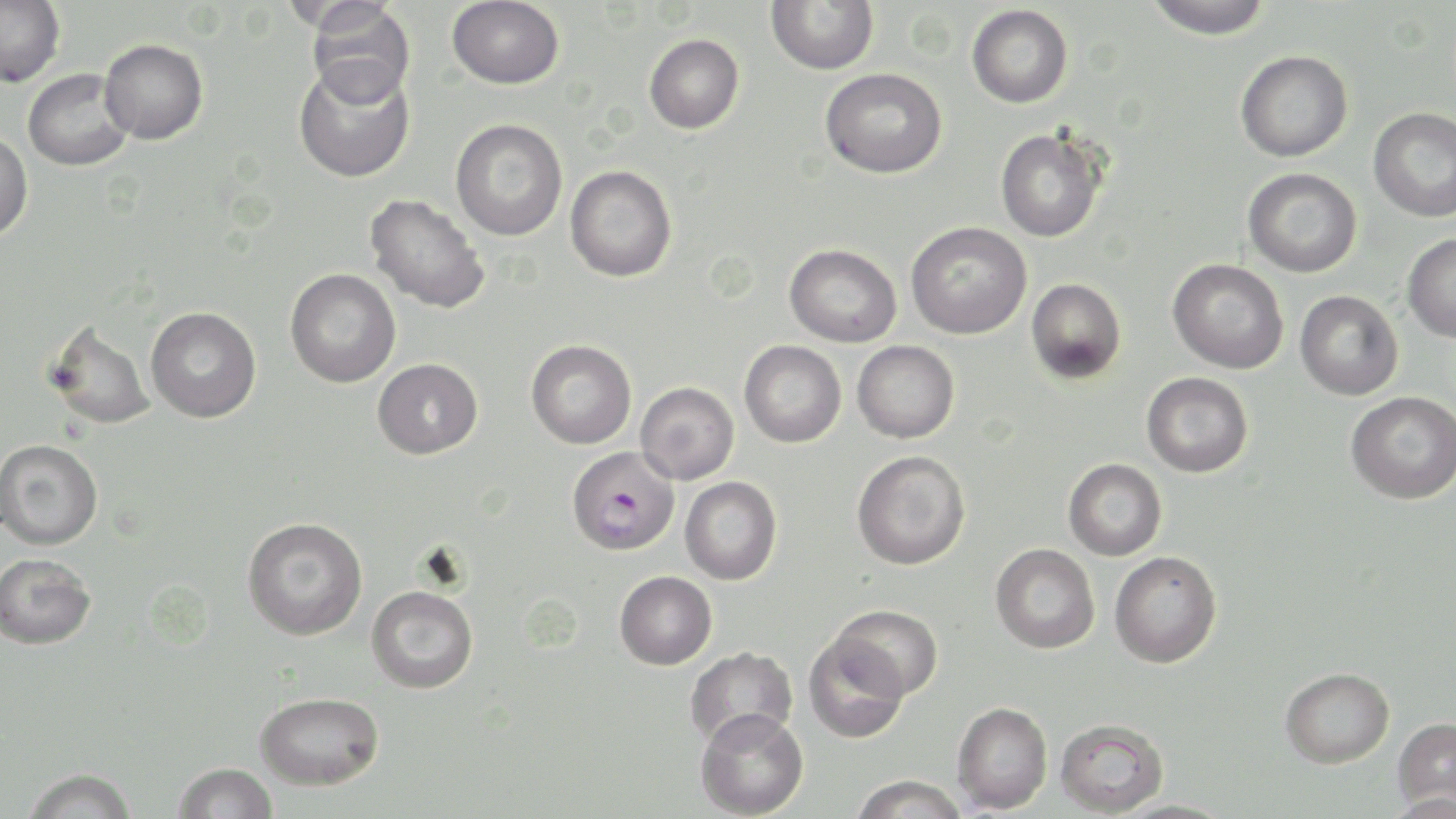
slide-level diagnosis = Plasmodium falciparum
modality = light microscopy
Plasmodium falciparum-infected red blood cell locations = approximate bounding boxes as (x1, y1, x2, y2) in pixels: (567, 446, 680, 556)
preparation = thin blood smear
magnification = 1000x
field of view = single
image size = 1456×819 pixels
stain = May-Grünwald-Giemsa
uninfected red blood cell locations = approximate bounding boxes as (x1, y1, x2, y2) in pixels: (447, 0, 564, 89), (766, 0, 879, 75), (1141, 0, 1274, 40), (0, 1, 65, 87), (305, 2, 416, 105), (966, 4, 1073, 108), (644, 33, 745, 133), (100, 39, 208, 144), (1235, 49, 1353, 162), (293, 62, 415, 183), (819, 67, 948, 178), (23, 68, 134, 171), (1369, 107, 1456, 222), (450, 118, 568, 241), (995, 127, 1108, 242), (0, 130, 33, 242), (565, 165, 677, 282), (1242, 167, 1362, 277), (364, 195, 490, 314), (906, 222, 1032, 339), (1402, 233, 1456, 343), (784, 244, 902, 348), (1167, 258, 1289, 374), (285, 269, 401, 388), (1026, 278, 1127, 384), (1295, 290, 1403, 400), (145, 307, 261, 423), (43, 319, 156, 430), (526, 340, 637, 449), (739, 340, 847, 448), (852, 340, 960, 443), (372, 359, 483, 459), (1141, 372, 1253, 477), (635, 382, 739, 485), (1346, 391, 1456, 504), (0, 439, 103, 550), (852, 450, 971, 570), (1063, 458, 1167, 560), (680, 476, 782, 585), (242, 517, 368, 640), (990, 543, 1099, 653), (1109, 551, 1222, 668), (0, 553, 97, 650), (614, 570, 717, 669), (366, 585, 478, 693), (829, 604, 944, 702), (803, 633, 910, 743), (685, 646, 798, 748), (1280, 667, 1394, 768), (255, 691, 384, 790), (952, 701, 1053, 813), (695, 708, 809, 818), (1392, 717, 1456, 811), (1055, 719, 1169, 817), (172, 762, 278, 819), (22, 767, 138, 819), (849, 774, 969, 818), (1114, 799, 1235, 818)